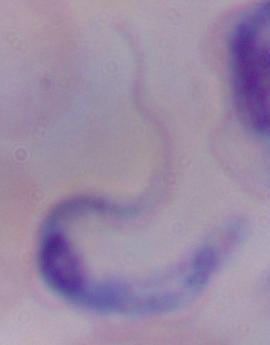

Micrograph. Captured at 1000x magnification. A trypanosome is seen.